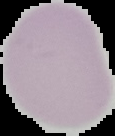 Result: no malaria parasites seen. Image is 115×136 pixels. Segmented cell region on a black background. From a thin blood film.